Assess this cell for malaria.
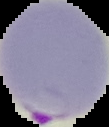
It is parasitized.

Image is 109×127 pixels. Cell region segmented out of the field of view; the surrounding area is masked to black. From a thin blood smear.